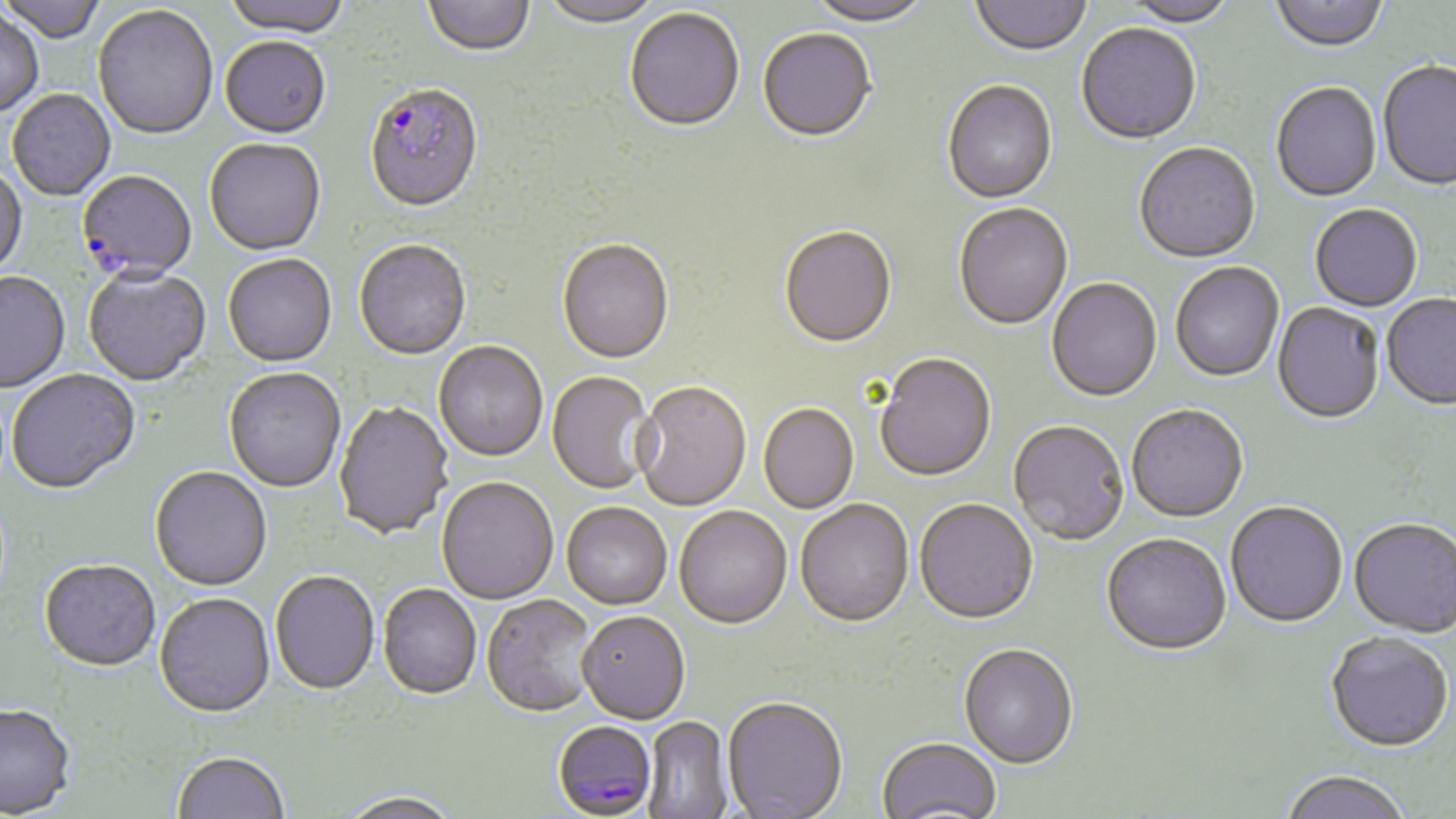
Approximate bounding boxes as (x1, y1, x2, y2) in pixels. Plasmodium falciparum-infected red blood cell locations: (364, 86, 484, 216), (76, 172, 197, 286), (551, 722, 664, 818). Uninfected red blood cell locations: (0, 0, 106, 45), (221, 0, 351, 41), (423, 0, 536, 58), (806, 0, 934, 29), (970, 0, 1092, 58), (1269, 0, 1388, 55), (538, 1, 664, 30), (1119, 1, 1237, 30), (93, 6, 218, 143), (0, 9, 44, 118), (625, 9, 745, 135), (1076, 25, 1201, 147), (758, 30, 877, 145), (220, 39, 331, 141), (1377, 62, 1456, 193), (942, 82, 1058, 206), (1271, 83, 1382, 204), (7, 90, 115, 202), (204, 140, 326, 258), (1134, 144, 1261, 265), (0, 166, 28, 280), (954, 204, 1073, 332), (1310, 206, 1422, 313), (780, 227, 897, 351), (354, 241, 472, 362), (556, 241, 674, 366), (223, 255, 337, 369), (1170, 263, 1284, 383), (83, 267, 212, 388), (0, 272, 70, 394), (1046, 279, 1162, 404), (1381, 295, 1456, 412), (1272, 303, 1385, 426), (434, 343, 548, 463), (875, 355, 997, 484), (6, 370, 141, 496), (224, 370, 346, 494), (547, 372, 657, 496), (633, 383, 751, 513), (333, 402, 453, 541), (758, 405, 859, 515), (1126, 407, 1248, 525), (1008, 422, 1129, 547), (150, 468, 272, 593), (436, 479, 559, 606), (795, 501, 914, 630), (914, 501, 1039, 627), (1225, 504, 1348, 630), (561, 505, 672, 612), (675, 508, 792, 631), (1349, 520, 1456, 640), (1101, 536, 1231, 659), (39, 562, 160, 674), (270, 573, 380, 698), (377, 585, 481, 701), (154, 595, 276, 721), (480, 596, 601, 720), (577, 614, 690, 727), (1326, 635, 1453, 755), (958, 646, 1078, 772), (722, 699, 848, 819), (0, 706, 76, 819), (642, 717, 733, 818), (877, 739, 1001, 819), (172, 753, 289, 818), (1279, 773, 1412, 819), (338, 794, 462, 819). Slide-level diagnosis: Plasmodium falciparum. Image is 1456×819 pixels. One field of a larger specimen. Captured at 1000x magnification. May-Grünwald-Giemsa-stained preparation. Thin blood film. Light microscopy.